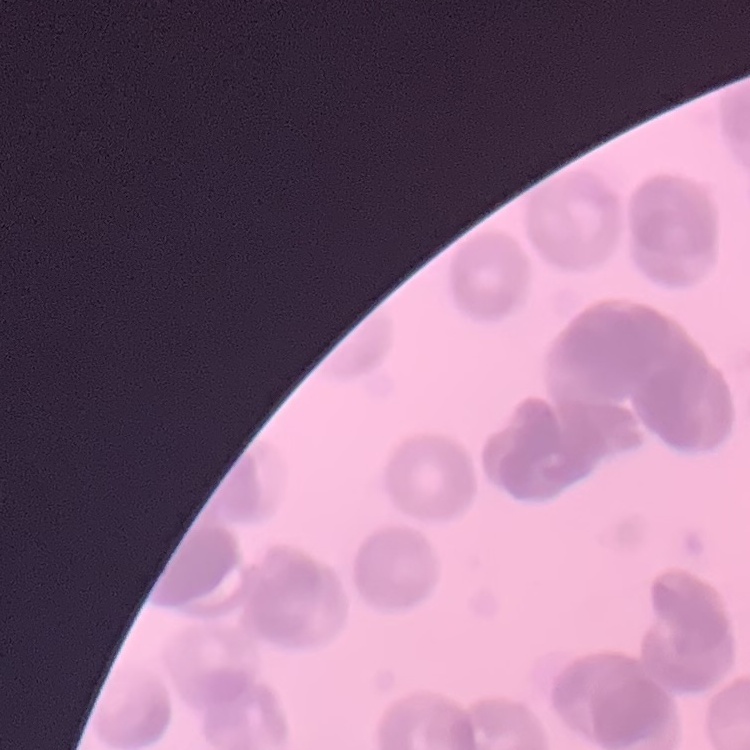

{
  "red_blood_cell_morphology": "rouleaux formation",
  "preparation": "thin blood film",
  "image_type": "square crop of a larger photomicrograph",
  "stain": "Field's or Giemsa"
}